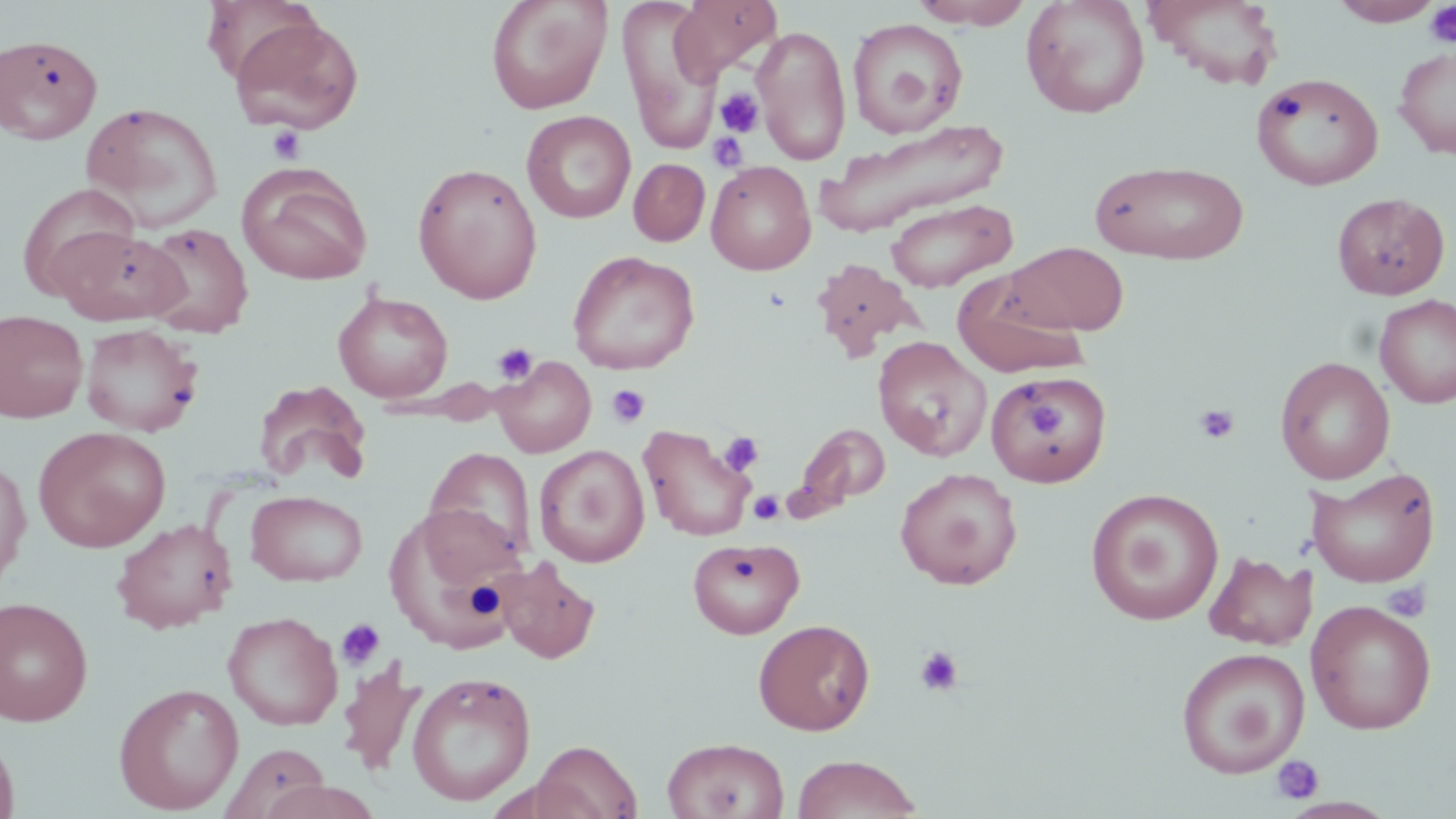

Summary:
  - Coordinate format: approximate bounding boxes as (x1, y1, x2, y2) in pixels
  - Platelet locations: (1424, 1, 1456, 48), (717, 88, 763, 137), (267, 125, 306, 165), (707, 132, 749, 173), (492, 343, 538, 385), (606, 384, 651, 428), (1026, 401, 1071, 442), (1194, 404, 1240, 444), (718, 431, 764, 477), (748, 491, 784, 525), (1382, 581, 1431, 623), (336, 619, 386, 670), (913, 645, 965, 697), (1271, 755, 1323, 805)
  - Uninfected red blood cell locations: (486, 0, 612, 114), (617, 0, 723, 154), (672, 0, 782, 80), (911, 0, 1033, 28), (1021, 0, 1150, 118), (1143, 0, 1285, 90), (1330, 0, 1444, 26), (229, 15, 365, 135), (847, 18, 967, 137), (753, 24, 851, 166), (0, 34, 103, 144), (1393, 47, 1456, 159), (1251, 72, 1384, 191), (80, 102, 223, 231), (521, 110, 636, 223), (817, 120, 1010, 237), (628, 158, 710, 246), (1090, 159, 1250, 264), (706, 160, 816, 275), (411, 161, 543, 304), (236, 163, 372, 286), (18, 182, 141, 299), (1332, 191, 1450, 300), (885, 198, 1016, 293), (1351, 215, 1456, 359), (140, 222, 254, 338), (52, 226, 187, 324), (1005, 242, 1129, 336), (567, 250, 700, 375), (810, 257, 921, 361), (952, 272, 1089, 379), (333, 292, 453, 403), (1374, 294, 1456, 410), (0, 310, 88, 423), (80, 323, 203, 437), (873, 337, 991, 462), (493, 356, 596, 457), (1275, 356, 1395, 485), (987, 370, 1113, 487), (253, 379, 372, 485), (793, 422, 890, 516), (639, 424, 755, 542), (33, 426, 171, 553), (534, 445, 649, 567), (423, 446, 538, 568), (0, 456, 31, 586), (895, 467, 1023, 590), (1307, 467, 1440, 588), (1086, 488, 1224, 625), (245, 490, 367, 586), (384, 504, 525, 656), (112, 518, 237, 634), (687, 537, 804, 639), (1204, 552, 1315, 650), (495, 558, 600, 664), (0, 596, 94, 726), (1305, 599, 1437, 735), (223, 611, 343, 730), (753, 619, 875, 735), (1174, 647, 1309, 778), (338, 661, 424, 776), (407, 671, 536, 806), (114, 682, 244, 814), (0, 729, 19, 819), (662, 737, 790, 819), (532, 740, 641, 819), (219, 742, 331, 819), (791, 754, 923, 819), (257, 780, 384, 819)
  - Slide-level diagnosis: negative for blood parasites
  - Magnification: 1000x
  - Image size: 1456×819 pixels
  - Modality: light microscopy
  - Stain: May-Grünwald-Giemsa
  - Field of view: single
  - Preparation: thin blood film